Comment on the morphology of the red blood cells.
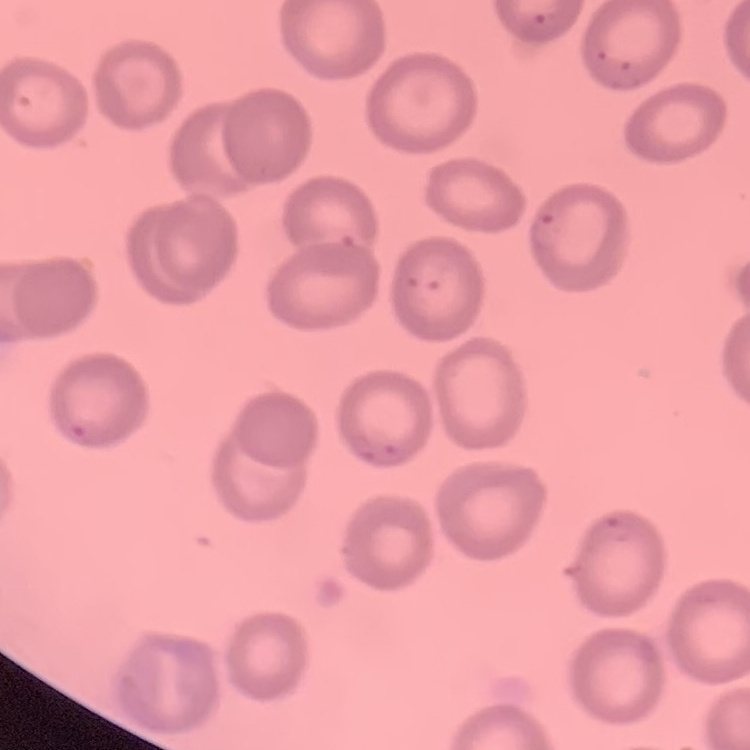
No rouleaux formation.

Summary:
  - Preparation: thin blood smear
  - Stain: Field's or Giemsa
  - Image type: square crop of a larger photomicrograph